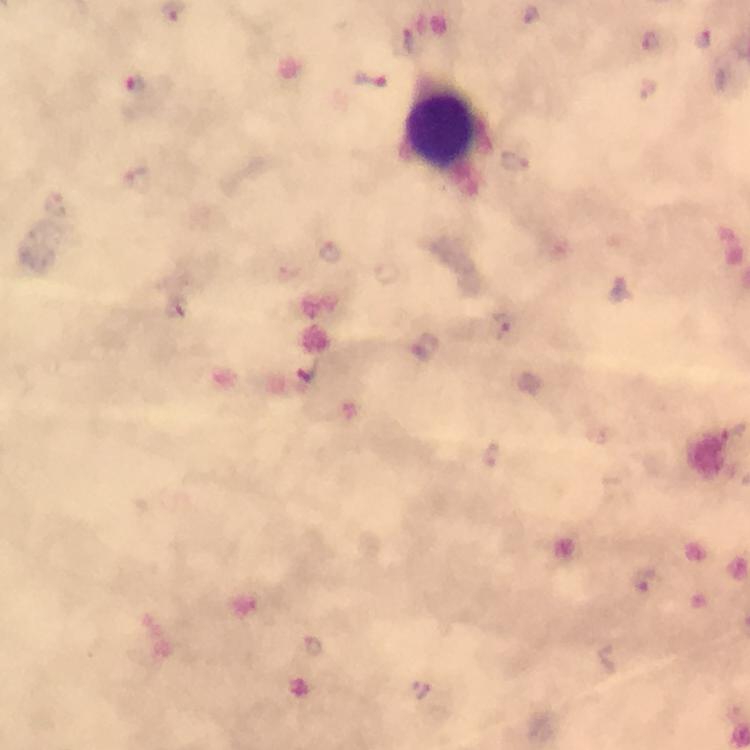

Approximate centers as (x, y) in pixels.
Summary:
  - Leukocyte locations: (439, 129)
  - Malaria parasite locations: (531, 14), (703, 38), (651, 41), (371, 80), (133, 84), (514, 158), (139, 181), (57, 206), (330, 251), (622, 289), (507, 328), (426, 348), (491, 453), (644, 580), (313, 645), (421, 689)
  - Preparation: thick blood film
  - Immersion oil: applied
  - Magnification: 100x
  - Stain: Giemsa
  - Image size: 750×750 pixels
  - Context: from a diagnostic examination for malaria
  - Capture: smartphone camera through the microscope
  - Cropped from: one field of view